Classify this cell by malaria status.
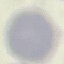
It is uninfected.

Summary:
  - Capture: smartphone camera at the microscope eyepiece
  - Image type: cell patch, automatically extracted from a larger field of view and resized to 64 × 64 pixels
  - Stain: Giemsa
  - Preparation: thin smear